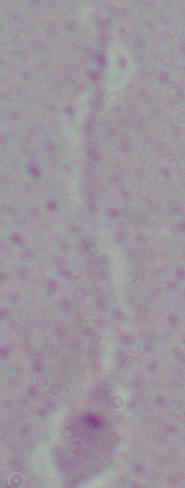

{
  "identification": "Leishmania",
  "modality": "micrograph",
  "magnification": "1000x"
}